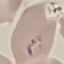

result: malaria parasites identified
capture: smartphone camera at the microscope eyepiece
preparation: thin blood film
image_type: cell patch, automatically extracted from a larger field of view and resized to 64 × 64 pixels
stain: Giemsa